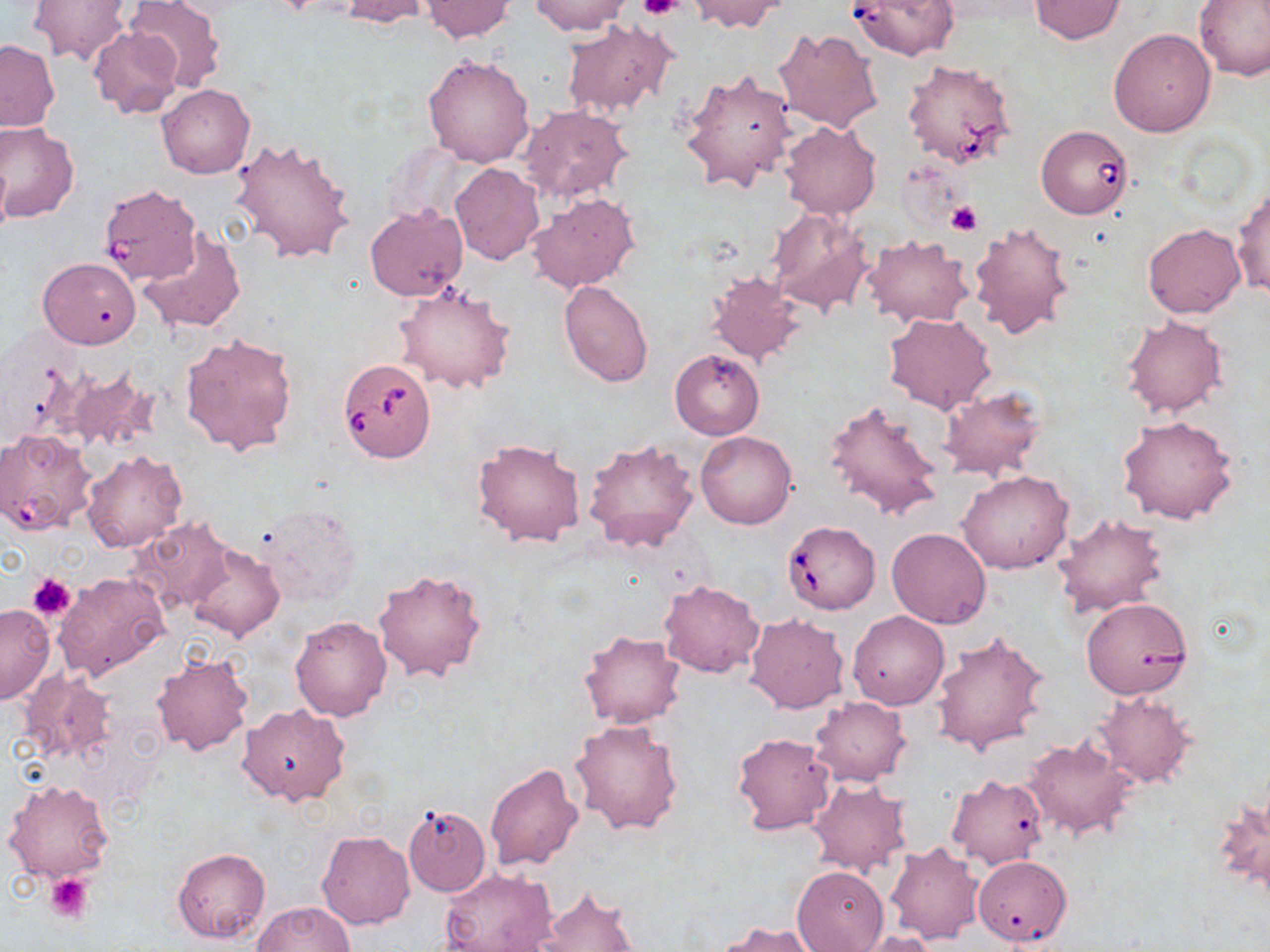

{
  "slide_level_diagnosis": "Babesia divergens",
  "image_size": "1270×952 pixels",
  "platelet_locations": "approximate bounding boxes as named x1/y1/x2/y2 corners in pixels: (x1=640, y1=0, x2=683, y2=22), (x1=946, y1=200, x2=981, y2=237), (x1=28, y1=573, x2=75, y2=621), (x1=44, y1=872, x2=95, y2=924)",
  "modality": "light microscopy",
  "babesia_divergens_infected_red_blood_cell_locations": "approximate bounding boxes as named x1/y1/x2/y2 corners in pixels: (x1=845, y1=0, x2=962, y2=63), (x1=902, y1=59, x2=1016, y2=169), (x1=1036, y1=123, x2=1134, y2=219), (x1=98, y1=183, x2=202, y2=286), (x1=338, y1=358, x2=436, y2=462), (x1=782, y1=520, x2=882, y2=614)",
  "uninfected_red_blood_cell_locations": "approximate bounding boxes as named x1/y1/x2/y2 corners in pixels: (x1=28, y1=0, x2=132, y2=66), (x1=124, y1=0, x2=226, y2=91), (x1=339, y1=0, x2=434, y2=26), (x1=688, y1=0, x2=786, y2=34), (x1=1029, y1=0, x2=1125, y2=43), (x1=1194, y1=0, x2=1270, y2=82), (x1=421, y1=1, x2=515, y2=42), (x1=530, y1=1, x2=632, y2=36), (x1=562, y1=20, x2=678, y2=118), (x1=87, y1=25, x2=184, y2=120), (x1=774, y1=27, x2=883, y2=133), (x1=1108, y1=28, x2=1215, y2=136), (x1=0, y1=39, x2=60, y2=131), (x1=422, y1=54, x2=535, y2=167), (x1=679, y1=70, x2=797, y2=192), (x1=157, y1=83, x2=255, y2=178), (x1=517, y1=104, x2=633, y2=203), (x1=780, y1=121, x2=881, y2=219), (x1=0, y1=123, x2=80, y2=223), (x1=230, y1=136, x2=355, y2=264), (x1=0, y1=153, x2=11, y2=241), (x1=450, y1=163, x2=544, y2=264), (x1=1231, y1=187, x2=1270, y2=299), (x1=528, y1=192, x2=639, y2=295), (x1=364, y1=204, x2=468, y2=300), (x1=766, y1=208, x2=875, y2=315), (x1=969, y1=219, x2=1077, y2=340), (x1=1142, y1=222, x2=1244, y2=318), (x1=138, y1=228, x2=246, y2=334), (x1=861, y1=235, x2=972, y2=328), (x1=37, y1=257, x2=141, y2=349), (x1=705, y1=271, x2=808, y2=368), (x1=391, y1=281, x2=515, y2=395), (x1=558, y1=281, x2=653, y2=387), (x1=883, y1=311, x2=996, y2=414), (x1=1121, y1=315, x2=1227, y2=418), (x1=180, y1=331, x2=298, y2=456), (x1=670, y1=349, x2=764, y2=439), (x1=61, y1=367, x2=161, y2=456), (x1=937, y1=387, x2=1046, y2=482), (x1=824, y1=397, x2=946, y2=524), (x1=1116, y1=416, x2=1241, y2=526), (x1=0, y1=429, x2=98, y2=534), (x1=695, y1=431, x2=797, y2=529), (x1=471, y1=437, x2=586, y2=548), (x1=584, y1=437, x2=700, y2=553), (x1=81, y1=449, x2=188, y2=554), (x1=958, y1=469, x2=1074, y2=574), (x1=255, y1=506, x2=360, y2=607), (x1=1053, y1=513, x2=1169, y2=619), (x1=129, y1=516, x2=233, y2=615), (x1=887, y1=527, x2=993, y2=628), (x1=184, y1=543, x2=284, y2=642), (x1=374, y1=567, x2=488, y2=682), (x1=54, y1=572, x2=171, y2=682), (x1=658, y1=581, x2=765, y2=678), (x1=1080, y1=599, x2=1191, y2=703), (x1=0, y1=604, x2=55, y2=704), (x1=847, y1=610, x2=949, y2=709), (x1=744, y1=613, x2=850, y2=713), (x1=290, y1=615, x2=392, y2=722), (x1=930, y1=628, x2=1051, y2=756), (x1=578, y1=629, x2=685, y2=729), (x1=150, y1=651, x2=254, y2=757), (x1=18, y1=668, x2=118, y2=767), (x1=1091, y1=691, x2=1195, y2=789), (x1=808, y1=696, x2=912, y2=786), (x1=237, y1=704, x2=350, y2=805), (x1=568, y1=718, x2=684, y2=836), (x1=731, y1=731, x2=836, y2=836), (x1=1023, y1=735, x2=1139, y2=840), (x1=484, y1=763, x2=584, y2=871), (x1=946, y1=774, x2=1049, y2=869), (x1=806, y1=778, x2=912, y2=876), (x1=3, y1=779, x2=115, y2=883), (x1=1212, y1=790, x2=1269, y2=903), (x1=402, y1=804, x2=492, y2=898), (x1=316, y1=831, x2=416, y2=930), (x1=885, y1=842, x2=983, y2=944), (x1=173, y1=847, x2=269, y2=944), (x1=972, y1=854, x2=1072, y2=947), (x1=791, y1=864, x2=888, y2=951), (x1=439, y1=868, x2=559, y2=952), (x1=533, y1=886, x2=638, y2=952), (x1=251, y1=902, x2=355, y2=952), (x1=715, y1=920, x2=825, y2=952), (x1=852, y1=931, x2=939, y2=952)",
  "magnification": "1000x",
  "preparation": "thin blood film",
  "field_of_view": "one of a larger specimen",
  "stain": "May-Grünwald-Giemsa"
}